Evaluate for parasitized red blood cells.
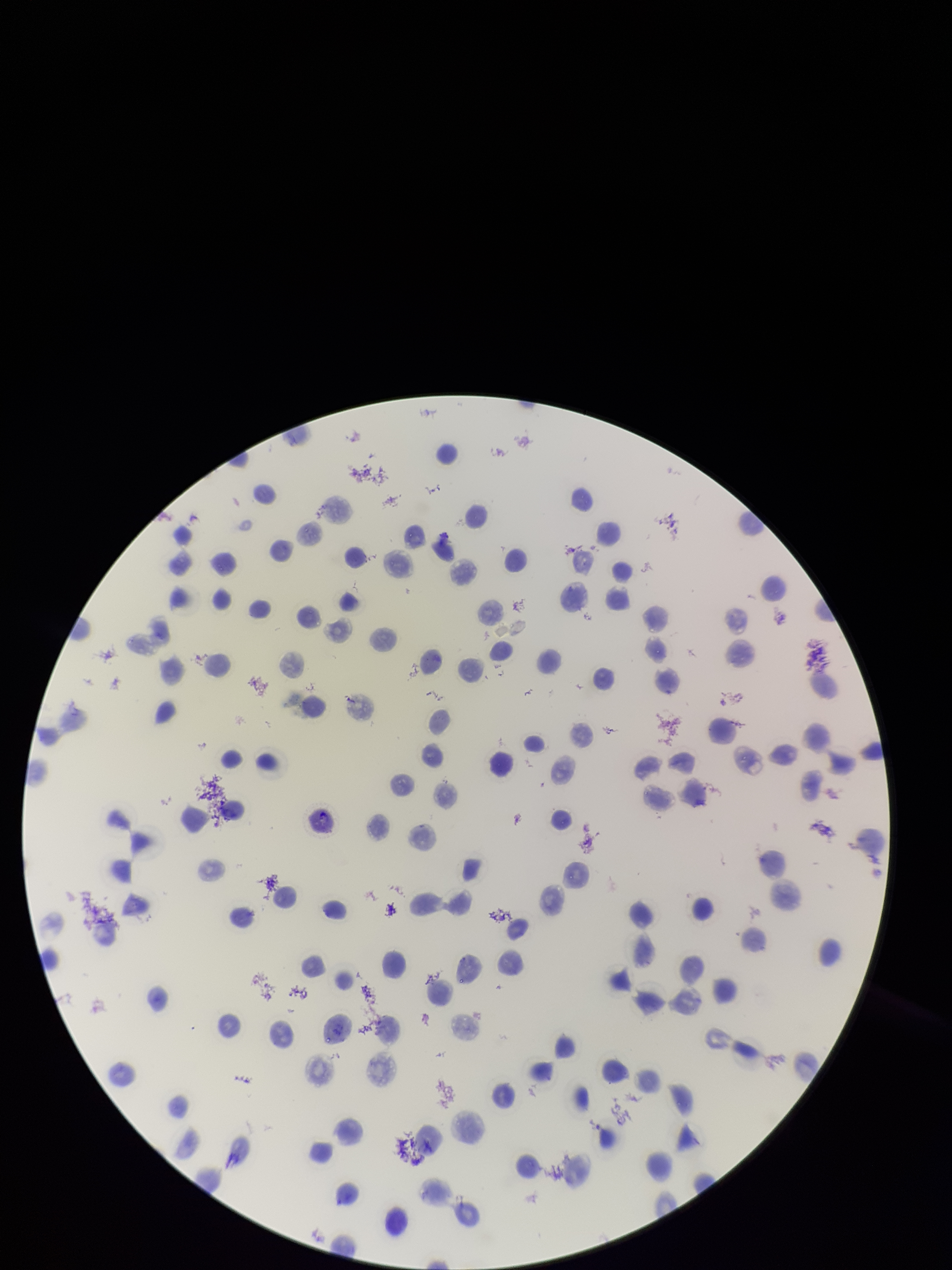
None detected.

stain = Giemsa
preparation = thin
species reported for this patient = Plasmodium vivax
red blood cell count = 118
image size = 952×1270 pixels
field of view = single
patient malaria status = infected
parasitized red blood cell count = 0
capture = smartphone photograph through the microscope eyepiece